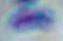
modality: micrograph
magnification: 1000x
identification: Toxoplasma gondii